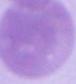

{
  "identification": "red blood cell",
  "magnification": "1000x",
  "modality": "photomicrograph"
}